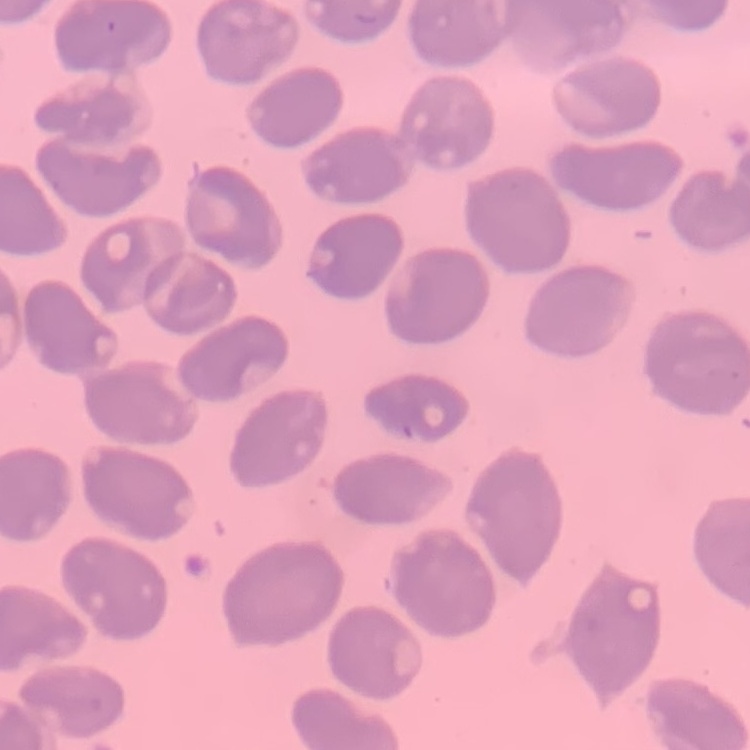
The erythrocytes exhibit no rouleaux formation. Field's or Giemsa stain. One tile cut from a larger photomicrograph. Thin blood smear.